Classify this cell by malaria status.
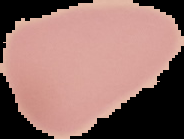

It is uninfected.

From a thin blood film. Image is 184×139 pixels. The area outside the segmented cell region is set to black.